Assess the morphology of the erythrocytes.
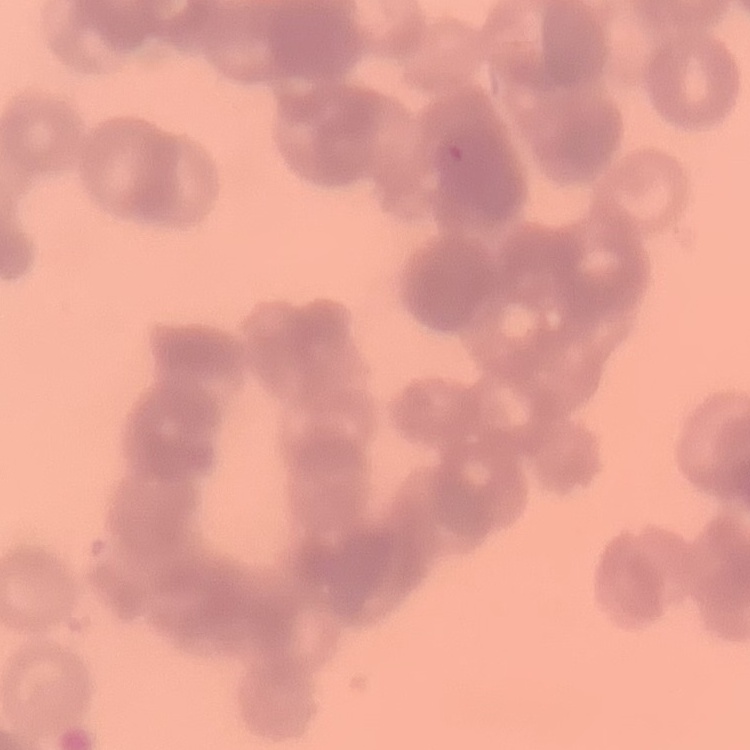

Rouleaux formation.

Summary:
  - Preparation: thin peripheral smear
  - Stain: Field's or Giemsa
  - Image type: one tile cut from a larger photomicrograph